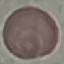

Summary:
  - Malaria status: uninfected
  - Preparation: thin blood smear
  - Image type: automatically extracted cell patch, resized to 64 × 64 pixels
  - Stain: Giemsa
  - Capture: smartphone through the microscope eyepiece